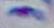

{
  "modality": "photomicrograph",
  "identification": "Toxoplasma gondii",
  "magnification": "1000x"
}